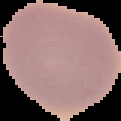

Summary:
  - Preparation: thin blood smear
  - Image size: 121×121 pixels
  - Malaria status: uninfected
  - Image type: cell region segmented out of the field of view; surrounding area masked to black